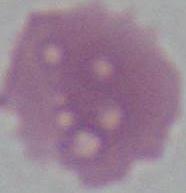

Summary:
  - Modality: photomicrograph
  - Magnification: 1000x
  - Identification: erythrocyte